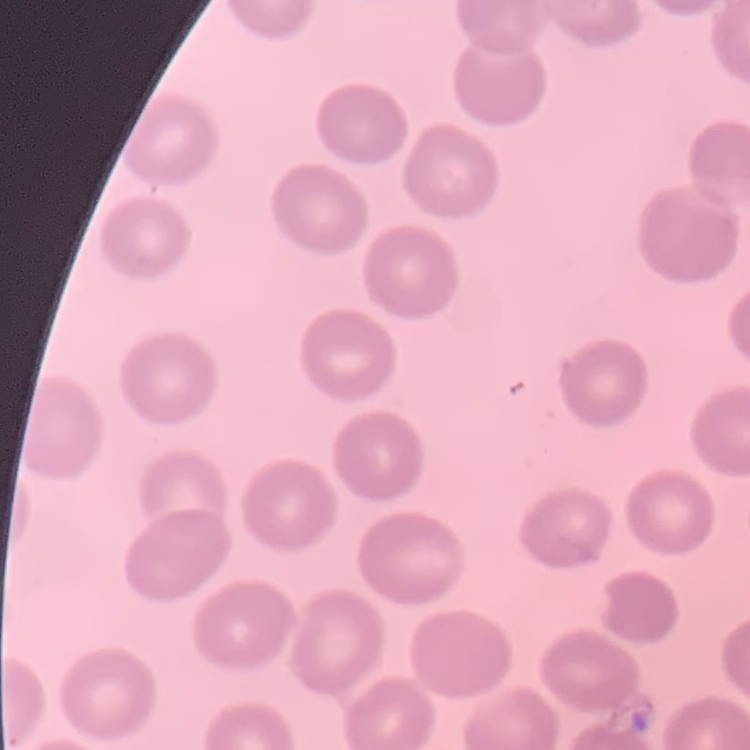
red blood cell morphology = no rouleaux formation
stain = Field's or Giemsa
image type = one tile cut from a larger photomicrograph
preparation = thin blood smear